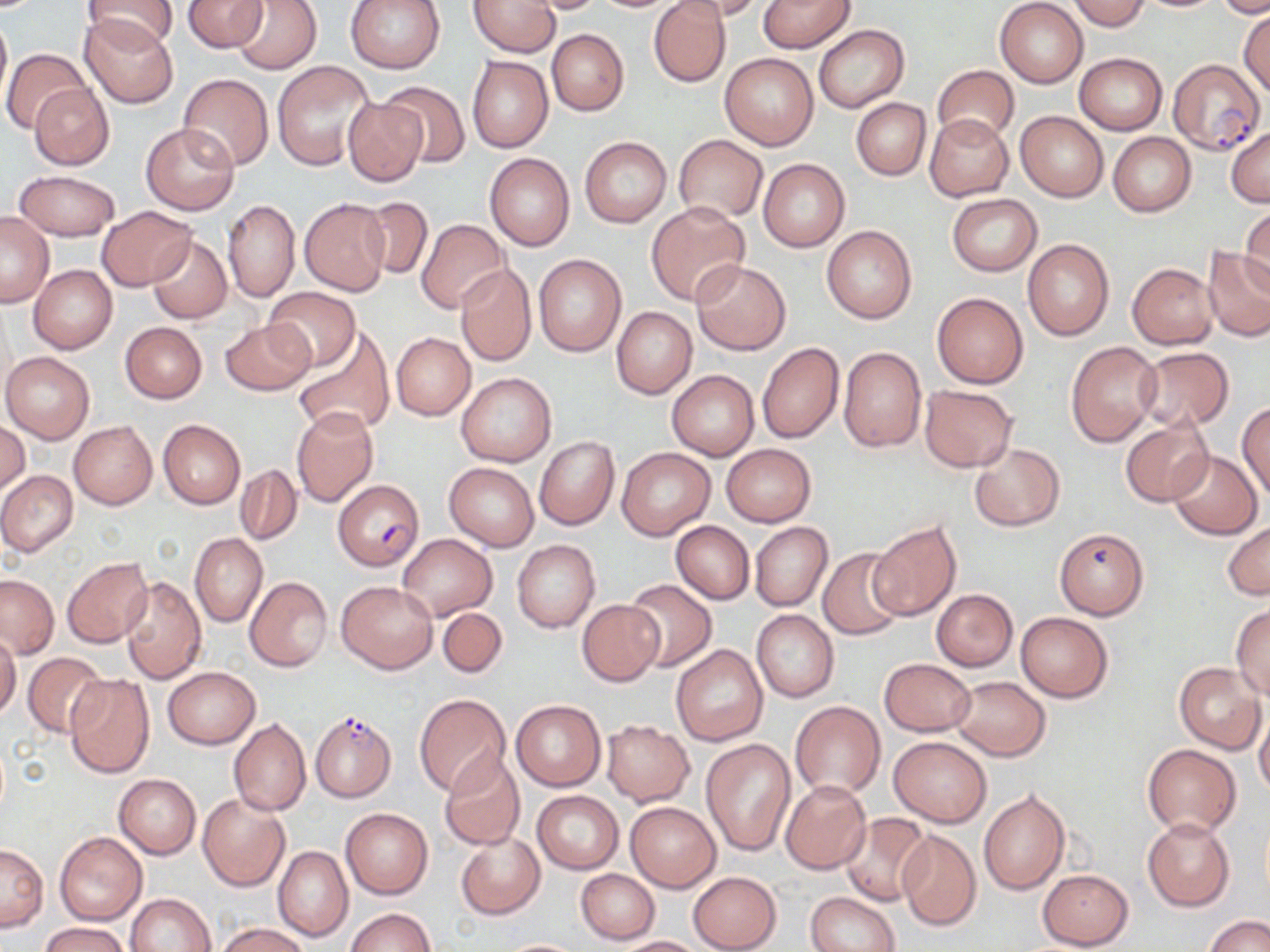
Summary:
  - Coordinate format: approximate bounding boxes as [x1, y1, x2, y2] in pixels
  - Uninfected red blood cell locations: [80, 0, 182, 52], [181, 0, 270, 52], [231, 0, 322, 74], [344, 0, 447, 74], [468, 0, 560, 57], [520, 0, 611, 14], [678, 0, 767, 21], [758, 0, 856, 52], [995, 0, 1089, 88], [1069, 0, 1150, 31], [1214, 0, 1270, 17], [648, 1, 732, 87], [1239, 7, 1270, 98], [0, 9, 11, 111], [78, 17, 178, 106], [813, 24, 909, 113], [545, 28, 629, 116], [2, 47, 91, 135], [719, 51, 819, 150], [1074, 53, 1168, 134], [467, 55, 553, 153], [272, 60, 374, 170], [931, 65, 1019, 146], [178, 74, 273, 170], [28, 82, 114, 169], [377, 82, 471, 168], [851, 97, 931, 180], [344, 99, 426, 186], [1015, 112, 1108, 201], [925, 113, 1013, 201], [140, 123, 239, 215], [1226, 125, 1270, 207], [1107, 132, 1196, 217], [674, 135, 768, 223], [579, 136, 671, 227], [484, 152, 574, 251], [758, 159, 850, 252], [13, 170, 120, 241], [947, 193, 1042, 276], [359, 196, 432, 282], [224, 199, 299, 302], [299, 199, 390, 295], [646, 203, 751, 306], [1239, 206, 1270, 296], [97, 207, 198, 291], [0, 212, 55, 307], [416, 218, 509, 313], [821, 225, 917, 323], [145, 235, 233, 326], [1023, 239, 1113, 341], [1203, 246, 1270, 342], [533, 254, 626, 356], [690, 258, 790, 355], [456, 263, 535, 366], [1127, 263, 1219, 349], [29, 264, 117, 353], [264, 288, 361, 372], [931, 291, 1029, 389], [611, 306, 697, 398], [220, 319, 316, 395], [120, 322, 207, 403], [292, 331, 396, 437], [391, 333, 475, 420], [1065, 341, 1161, 446], [757, 342, 844, 443], [838, 346, 927, 453], [1133, 347, 1235, 432], [2, 352, 94, 442], [666, 370, 759, 459], [457, 371, 556, 467], [920, 384, 1017, 471], [1237, 402, 1270, 503], [291, 408, 378, 507], [158, 419, 245, 508], [1121, 419, 1214, 508], [0, 420, 29, 496], [69, 420, 157, 510], [534, 436, 620, 530], [720, 442, 817, 527], [968, 443, 1064, 532], [617, 448, 714, 539], [1166, 450, 1262, 540], [444, 462, 538, 550], [235, 465, 301, 545], [0, 470, 77, 557], [670, 521, 754, 604], [1223, 521, 1269, 600], [750, 522, 832, 612], [868, 522, 962, 622], [1054, 528, 1149, 619], [189, 532, 267, 627], [397, 533, 497, 621], [512, 540, 600, 632], [817, 548, 909, 641], [62, 559, 152, 647], [1, 573, 59, 659], [121, 575, 206, 683], [244, 576, 333, 671], [622, 579, 716, 672], [336, 581, 438, 673], [933, 587, 1022, 758], [931, 589, 1018, 671], [577, 599, 664, 687], [1230, 602, 1270, 699], [437, 606, 508, 679], [751, 610, 839, 702], [1015, 612, 1114, 702], [0, 631, 21, 721], [671, 644, 768, 747], [22, 652, 106, 738], [879, 658, 975, 736], [1174, 661, 1266, 754], [162, 666, 260, 749], [64, 672, 154, 777], [951, 676, 1050, 761], [414, 693, 511, 797], [511, 700, 605, 791], [789, 701, 885, 798], [1254, 707, 1270, 799], [228, 718, 310, 816], [601, 720, 694, 805], [888, 736, 992, 827], [701, 739, 795, 856], [1141, 744, 1242, 837], [437, 755, 526, 850], [114, 774, 201, 858], [781, 781, 871, 872], [978, 789, 1068, 896], [531, 790, 623, 873], [197, 793, 290, 892], [625, 801, 720, 891], [340, 808, 433, 898], [839, 813, 934, 906], [1142, 817, 1235, 912], [895, 829, 981, 931], [54, 831, 146, 925], [454, 832, 545, 919], [0, 842, 47, 931], [273, 845, 352, 942], [576, 868, 660, 944], [1037, 869, 1133, 949], [687, 871, 782, 952], [127, 892, 215, 952], [806, 892, 900, 952], [346, 908, 435, 951], [1203, 914, 1269, 952], [39, 921, 130, 952], [216, 923, 311, 952], [611, 935, 707, 952], [495, 939, 588, 951]
  - Plasmodium falciparum-infected red blood cell locations: [1167, 58, 1264, 155], [331, 480, 423, 570], [310, 711, 396, 802]
  - Slide-level diagnosis: Plasmodium falciparum
  - Image size: 1270×952 pixels
  - Preparation: thin blood film
  - Modality: light microscopy
  - Field of view: one of a larger specimen
  - Stain: May-Grünwald-Giemsa
  - Magnification: 1000x